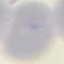

Result: no malaria parasites detected. Giemsa stain. Automatically extracted cell patch, resized to 64 × 64 pixels. Thin smear of blood. Photographed with a smartphone camera at the microscope eyepiece.